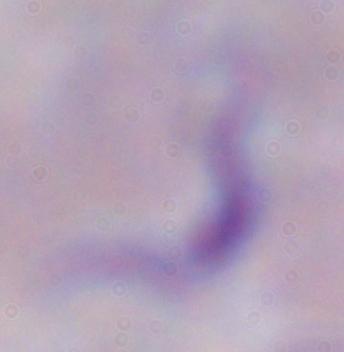
Micrograph. A trypanosome is seen. 1000x magnification.